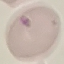
malaria status = uninfected
image type = automatically extracted cell patch, resized to 64 × 64 pixels
capture = smartphone camera at the microscope eyepiece
preparation = thin smear
stain = Giemsa